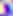

{
  "modality": "photomicrograph",
  "magnification": "400x",
  "identification": "Toxoplasma gondii"
}